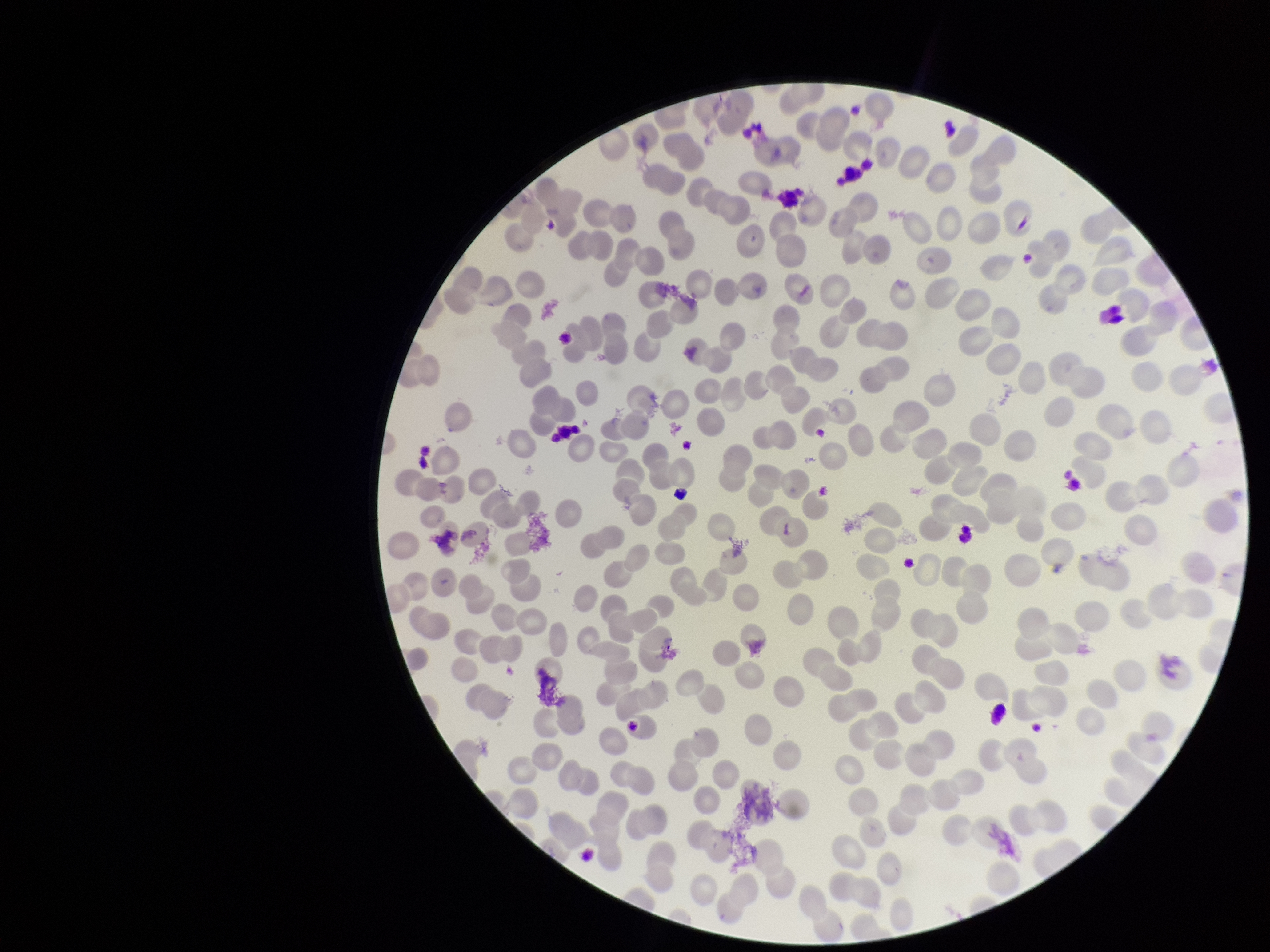

field of view = single
stain = Giemsa
parasitized red blood cell count = 0
red blood cell count = 234
preparation = thin
image size = 1270×952 pixels
parasitized red blood cells = none detected
capture = smartphone photograph through the microscope eyepiece
patient malaria status = negative